Locate every Plasmodium parasite.
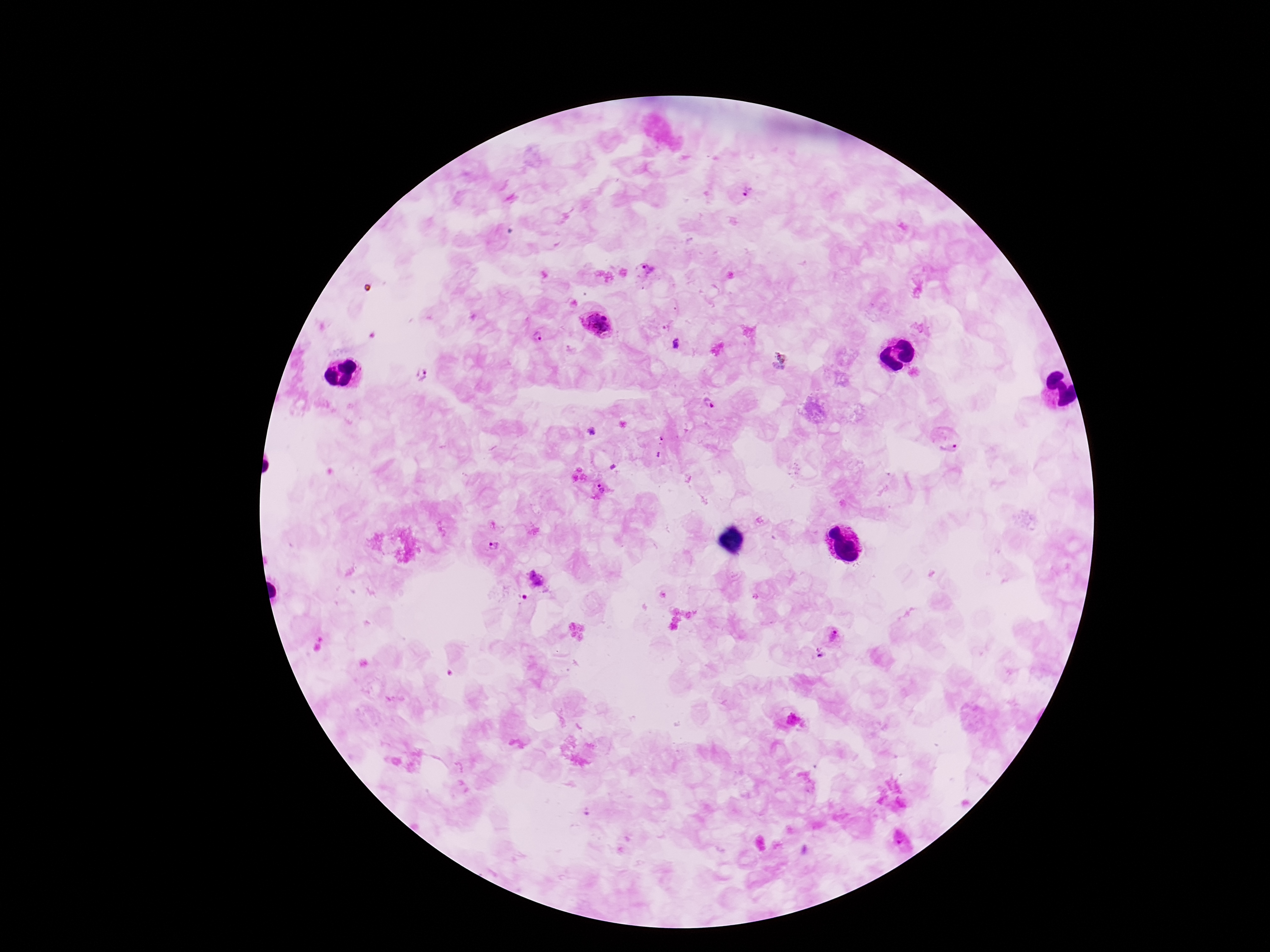

Approximate centers as (x, y) in pixels.
Plasmodium parasites: (746, 192), (644, 271), (596, 322), (538, 336), (676, 342), (421, 376), (708, 403), (950, 440), (658, 447), (598, 489), (492, 547), (535, 588), (834, 636), (795, 723).

patient malaria status = positive
preparation = thick peripheral-blood smear
magnification = 100x
stain = Giemsa
field of view = one from this slide
image size = 1270×952 pixels
capture = smartphone camera through the microscope eyepiece